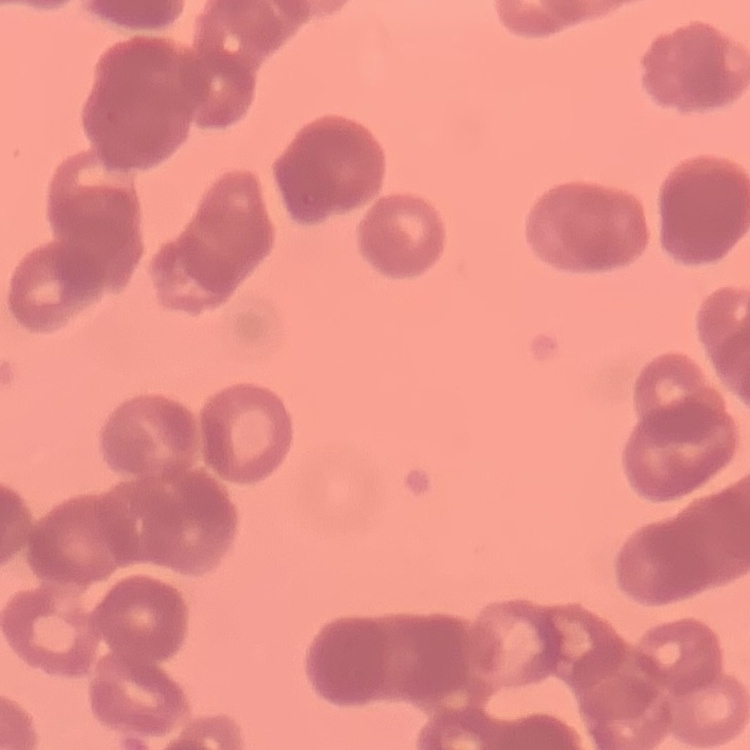

{
  "erythrocyte_morphology": "rouleaux formation",
  "preparation": "thin blood film",
  "image_type": "square crop of a larger photomicrograph",
  "stain": "Field's or Giemsa"
}